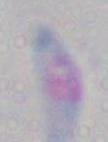
1000x magnification. Micrograph. Toxoplasma gondii is shown.